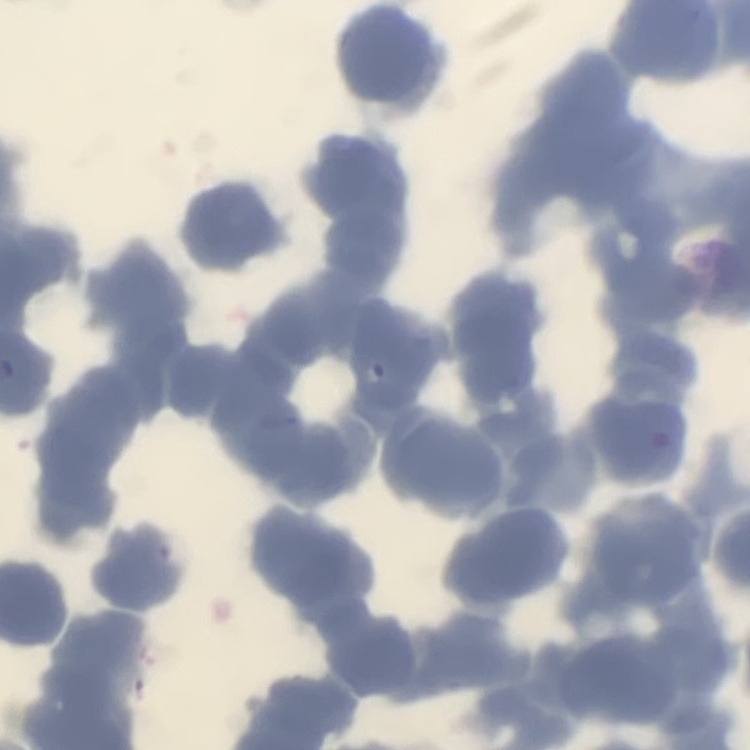 The erythrocytes show rouleaux formation. Thin blood smear. Field's or Giemsa stain. One tile cut from a larger photomicrograph.